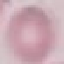

result = no malaria parasites seen
stain = Giemsa
capture = smartphone through the microscope eyepiece
preparation = thin blood film
image type = automatically extracted cell patch, resized to 64 × 64 pixels